Describe the morphology of the erythrocytes.
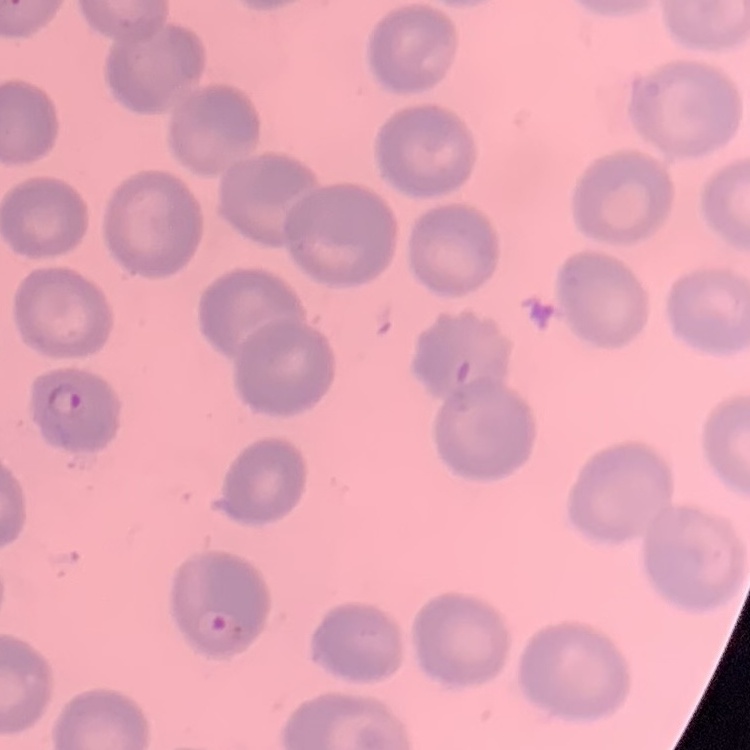

No rouleaux formation.

Summary:
  - Stain: Field's or Giemsa
  - Preparation: thin peripheral smear
  - Image type: one tile cut from a larger photomicrograph